Comment on the morphology of the red blood cells.
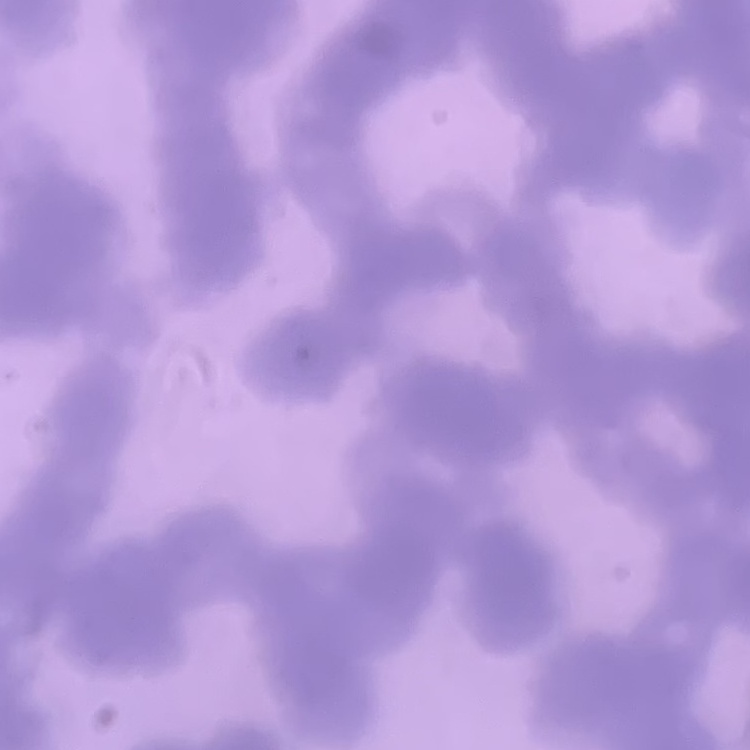
They show rouleaux formation.

Summary:
  - Preparation: thin peripheral smear
  - Stain: Field's or Giemsa
  - Image type: square crop of a larger photomicrograph